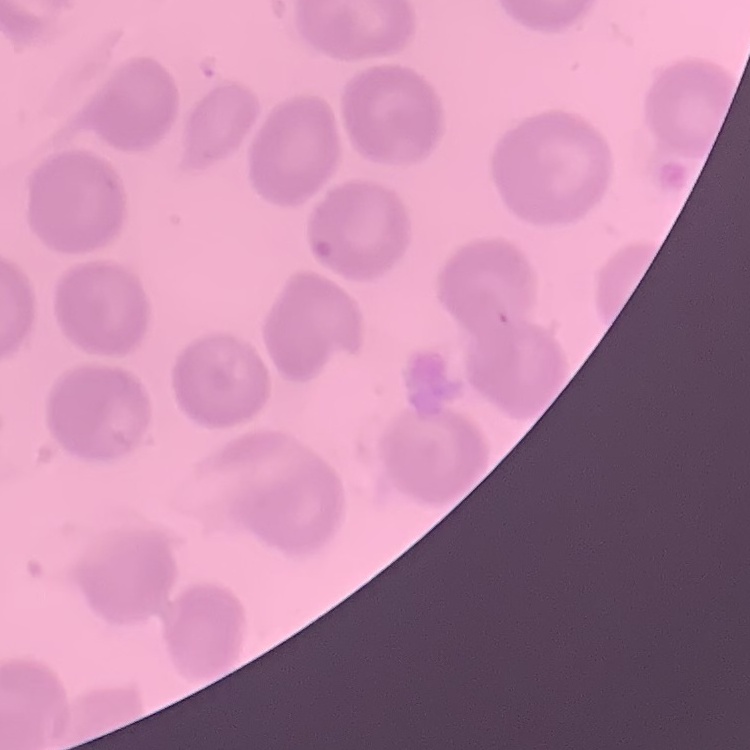
The erythrocytes exhibit no rouleaux formation. Stained with either Field's or Giemsa. Thin peripheral smear. Square crop of a larger photomicrograph.